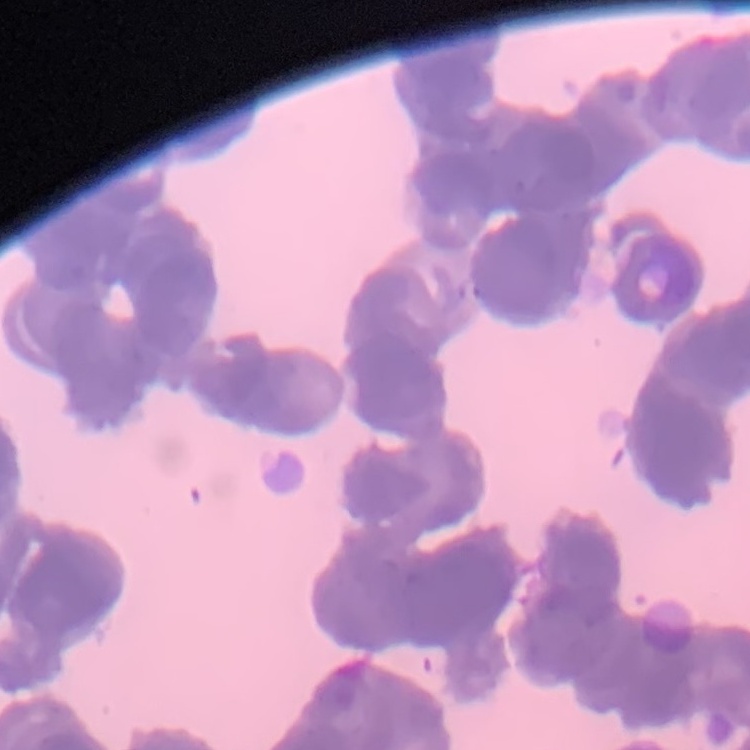

The erythrocytes exhibit rouleaux formation. One tile cut from a larger photomicrograph. Thin blood smear. Stained with either Field's or Giemsa.